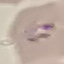

result = negative for malaria parasites
capture = smartphone through the microscope eyepiece
preparation = thin blood smear
stain = Giemsa
image type = cell patch, automatically extracted from a larger field of view and resized to 64 × 64 pixels